Describe the morphology of the red blood cells.
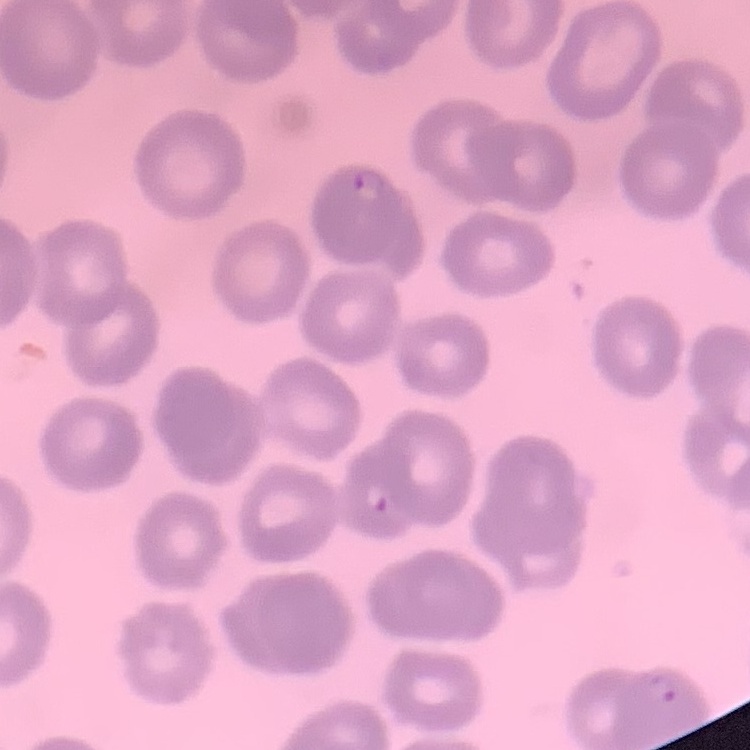
No rouleaux formation.

Field's or Giemsa stain. One tile cut from a larger photomicrograph. Thin blood smear.